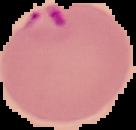
Summary:
  - Image size: 136×130 pixels
  - Preparation: thin blood smear
  - Image type: segmented cell region with the area outside set to black
  - Result: malaria parasites detected